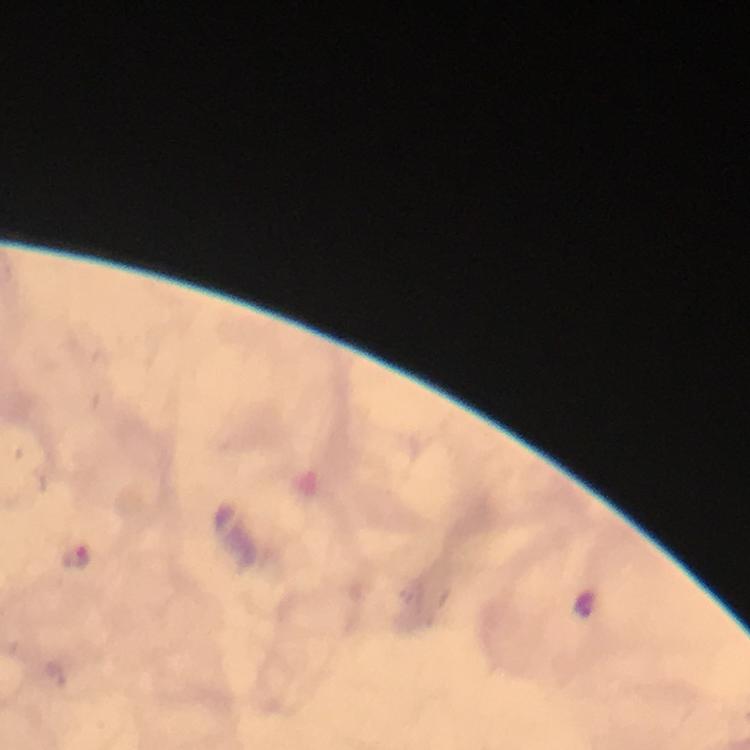
Approximate centers as (x, y) in pixels.
Summary:
  - Malaria parasite locations: (75, 556)
  - Immersion oil: applied
  - Capture: smartphone mounted on the microscope
  - Context: from a diagnostic examination for malaria
  - Stain: Giemsa
  - Image size: 750×750 pixels
  - Magnification: 100x
  - Cropped from: a single field of view
  - Preparation: thick blood smear